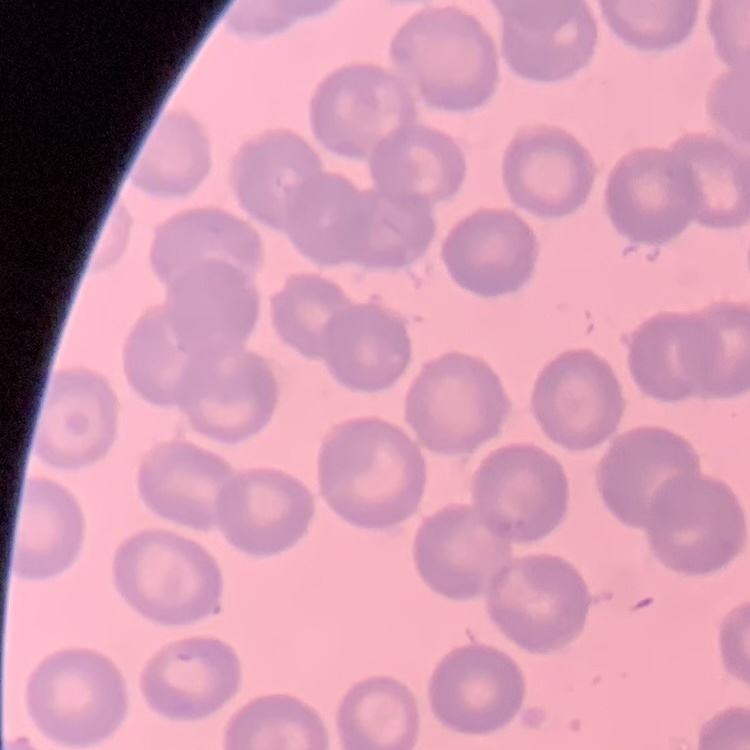

Summary:
  - Red blood cell morphology: no rouleaux formation
  - Preparation: thin blood smear
  - Image type: square crop of a larger photomicrograph
  - Stain: Field's or Giemsa